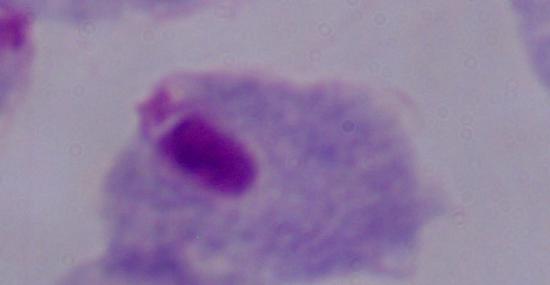

Photomicrograph. 1000x magnification. A trichomonad is shown.